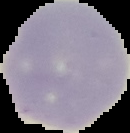
Summary:
  - Result: no malaria parasites detected
  - Image type: segmented cell region on a black background
  - Image size: 130×133 pixels
  - Preparation: thin blood film